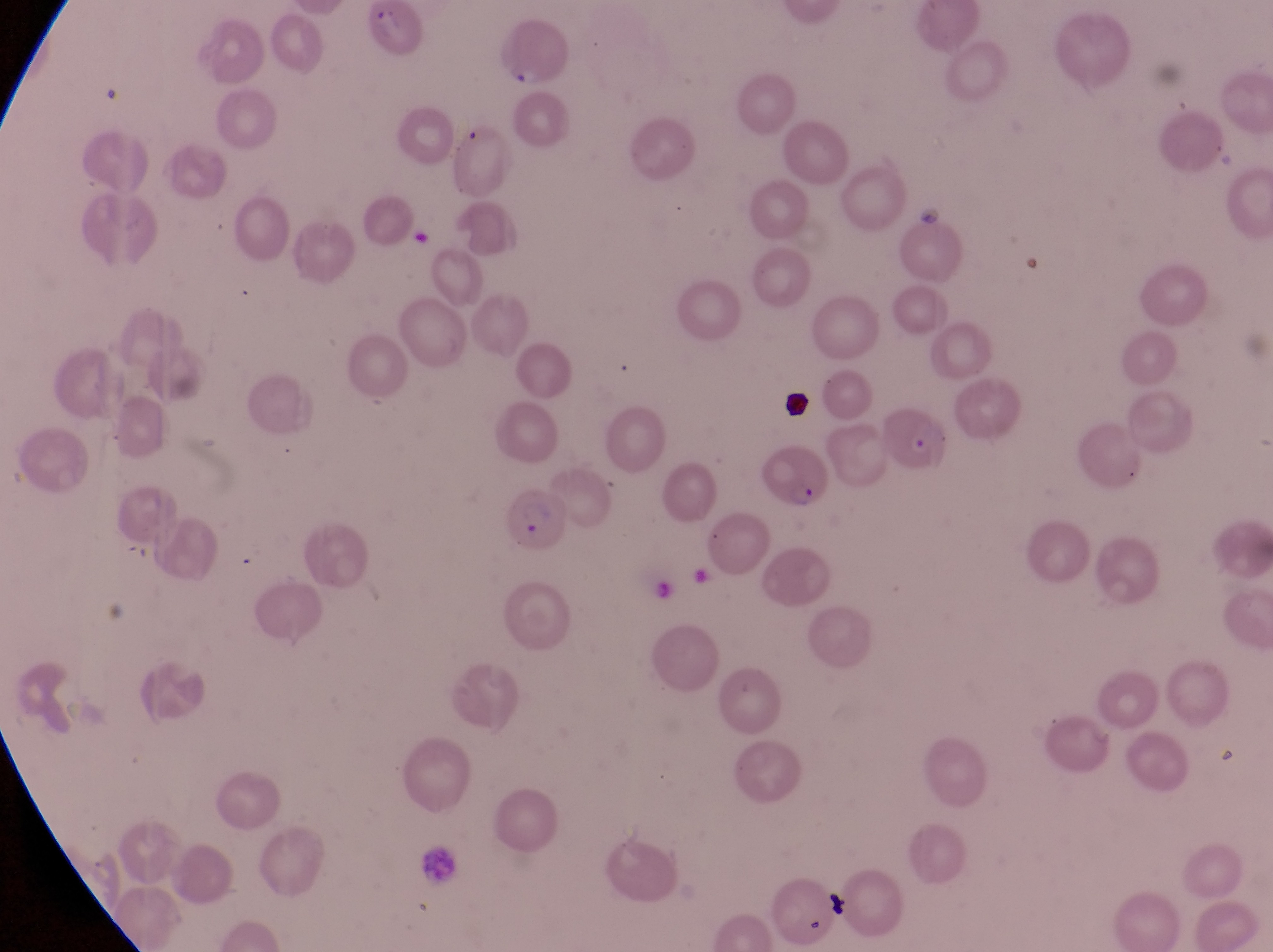

Approximate bounding boxes as left top right bottom in pixels.
Summary:
  - Leukocyte locations: 413 844 461 886
  - Artifact (platelet-like body, stain precipitate, or debris) locations: 776 392 813 421; 824 889 851 921
  - Parasitised red blood cell locations: 874 405 956 477; 759 445 831 507; 507 492 572 555
  - Magnification: 1000x
  - Field of view: single
  - Preparation: thin blood film
  - Country: Uganda
  - Capture: smartphone photograph through the eyepiece of an Olympus CX-23 microscope
  - Image size: 1273×952 pixels